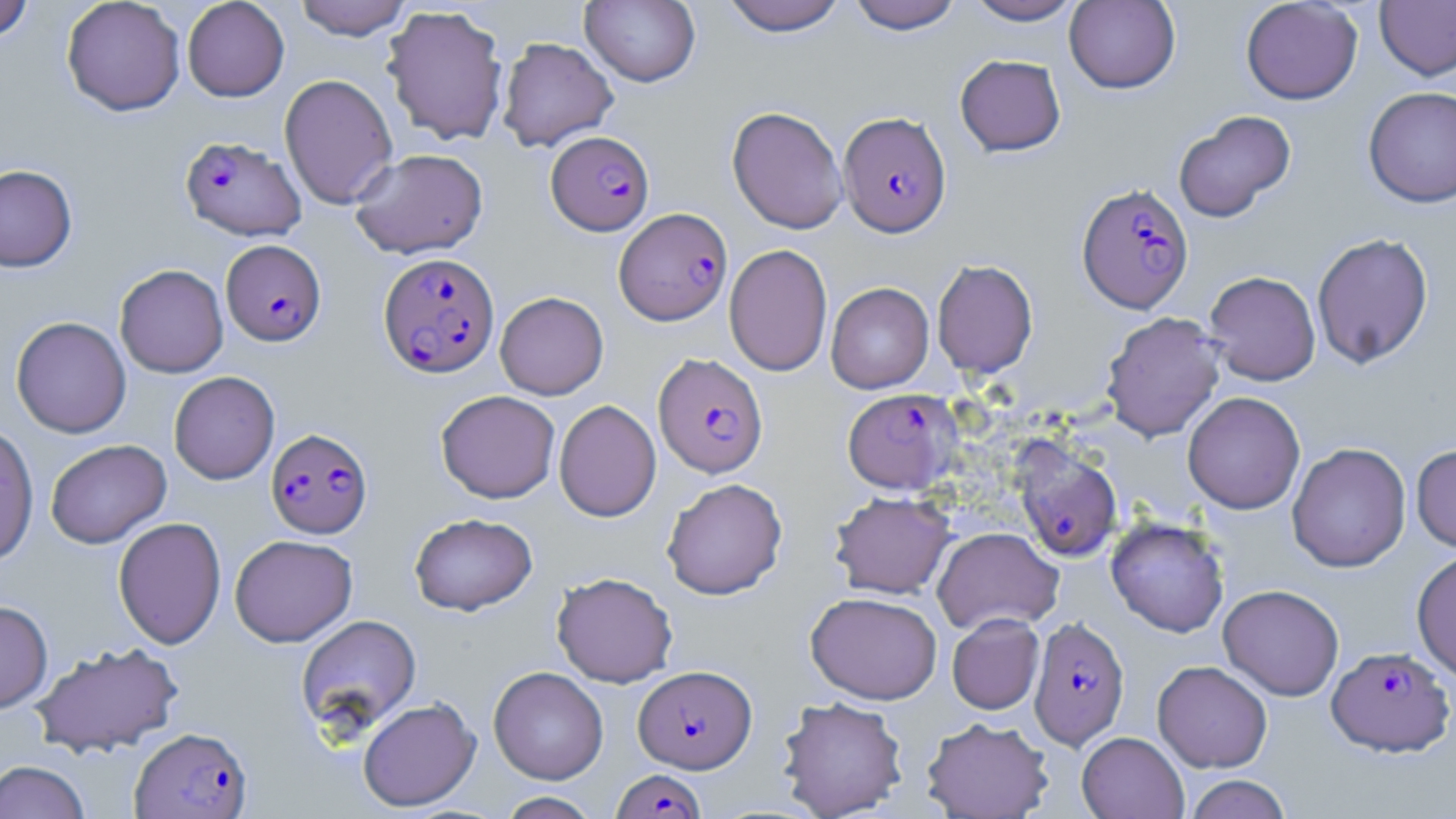

slide_level_diagnosis: Plasmodium falciparum
modality: optical microscopy
plasmodium_falciparum_infected_red_blood_cell_locations: 'approximate bounding boxes as (x1, y1, x2, y2) in pixels: (838, 111, 951, 237), (545, 131, 654, 235), (180, 135, 306, 241), (1077, 183, 1193, 313), (615, 207, 732, 326), (221, 240, 326, 345), (378, 253, 499, 378), (653, 353, 768, 478), (847, 383, 964, 489), (266, 427, 373, 538), (1013, 441, 1122, 562), (1029, 616, 1129, 749), (1327, 645, 1454, 757), (634, 665, 757, 773), (130, 727, 252, 818), (612, 769, 704, 818)'
uninfected_red_blood_cell_locations: 'approximate bounding boxes as (x1, y1, x2, y2) in pixels: (61, 0, 186, 117), (182, 0, 290, 101), (293, 0, 412, 40), (580, 0, 701, 87), (719, 0, 848, 36), (846, 0, 964, 34), (964, 0, 1085, 25), (1241, 0, 1363, 104), (0, 1, 35, 42), (1064, 1, 1181, 94), (1375, 1, 1456, 80), (381, 5, 509, 146), (497, 36, 619, 151), (955, 53, 1066, 156), (279, 73, 398, 209), (1363, 86, 1456, 208), (727, 106, 848, 234), (1172, 110, 1296, 222), (349, 148, 488, 259), (0, 164, 77, 272), (1311, 232, 1434, 369), (724, 244, 832, 376), (932, 259, 1038, 378), (114, 264, 228, 378), (1204, 270, 1321, 385), (825, 282, 934, 393), (495, 291, 609, 399), (1101, 311, 1226, 441), (11, 316, 131, 438), (168, 371, 280, 484), (435, 390, 560, 503), (1182, 391, 1305, 514), (554, 399, 661, 522), (0, 422, 39, 566), (45, 439, 171, 548), (1287, 442, 1411, 572), (1411, 444, 1456, 552), (661, 478, 787, 600), (830, 491, 955, 599), (409, 512, 537, 616), (113, 516, 226, 649), (1106, 517, 1230, 637), (933, 526, 1064, 634), (230, 534, 357, 647), (1412, 550, 1456, 681), (551, 572, 678, 687), (1218, 584, 1344, 700), (805, 591, 942, 704), (0, 600, 53, 713), (947, 613, 1044, 714), (296, 614, 421, 736), (30, 640, 185, 757), (1153, 660, 1273, 772), (488, 666, 608, 784), (777, 695, 909, 818), (357, 698, 481, 812), (921, 716, 1054, 818), (1077, 731, 1188, 819), (0, 760, 91, 819), (1183, 774, 1293, 819), (496, 792, 601, 818)'
preparation: thin blood film
image_size: 1456×819 pixels
field_of_view: single
stain: May-Grünwald-Giemsa
magnification: 1000x